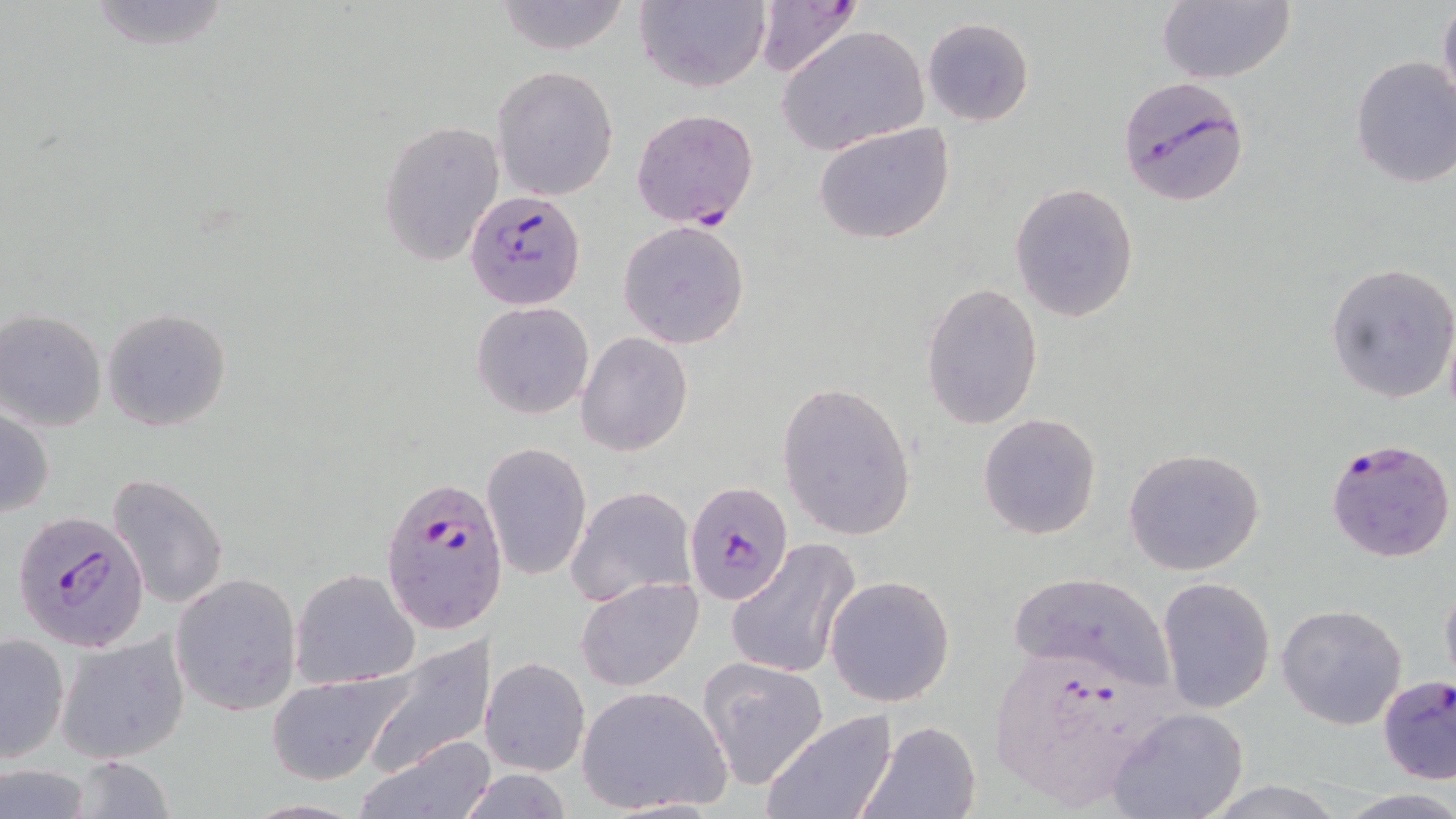

slide-level diagnosis = Plasmodium falciparum
preparation = thin blood film
modality = light microscopy
Plasmodium falciparum-infected red blood cell locations = approximate bounding boxes as [x1, y1, x2, y2] in pixels: [751, 1, 862, 79], [1118, 79, 1252, 208], [630, 107, 760, 230], [464, 191, 586, 310], [1325, 437, 1455, 564], [378, 474, 505, 636], [684, 480, 793, 605], [13, 512, 150, 651], [988, 646, 1182, 808], [1377, 675, 1456, 785]
field of view = single
stain = May-Grünwald-Giemsa
image size = 1456×819 pixels
uninfected red blood cell locations = approximate bounding boxes as [x1, y1, x2, y2] in pixels: [82, 0, 237, 54], [492, 0, 634, 54], [635, 0, 770, 93], [1155, 0, 1298, 86], [1438, 0, 1456, 116], [921, 17, 1035, 126], [776, 24, 930, 155], [1350, 55, 1456, 190], [491, 67, 618, 199], [378, 119, 504, 265], [812, 122, 955, 246], [1010, 183, 1139, 323], [617, 220, 750, 350], [1326, 261, 1456, 403], [919, 281, 1045, 431], [471, 301, 594, 418], [101, 307, 232, 432], [1, 310, 107, 431], [576, 332, 694, 456], [777, 380, 918, 540], [0, 407, 55, 518], [977, 412, 1103, 540], [482, 441, 592, 581], [1123, 447, 1266, 576], [107, 473, 228, 611], [566, 486, 696, 609], [725, 539, 860, 682], [291, 568, 419, 690], [1006, 572, 1171, 686], [825, 573, 956, 707], [172, 574, 300, 715], [1440, 574, 1456, 696], [577, 576, 705, 690], [1157, 576, 1275, 714], [1276, 604, 1408, 731], [56, 631, 191, 764], [1, 632, 70, 761], [361, 639, 494, 779], [481, 657, 590, 775], [697, 657, 829, 789], [265, 669, 415, 786], [577, 685, 733, 815], [1109, 708, 1249, 819], [760, 711, 896, 819], [859, 720, 981, 819], [356, 737, 494, 819], [65, 756, 178, 818], [1, 764, 95, 818], [452, 771, 577, 818], [1333, 789, 1456, 818]
magnification = 1000x